Locate every blood parasite and identify its species.
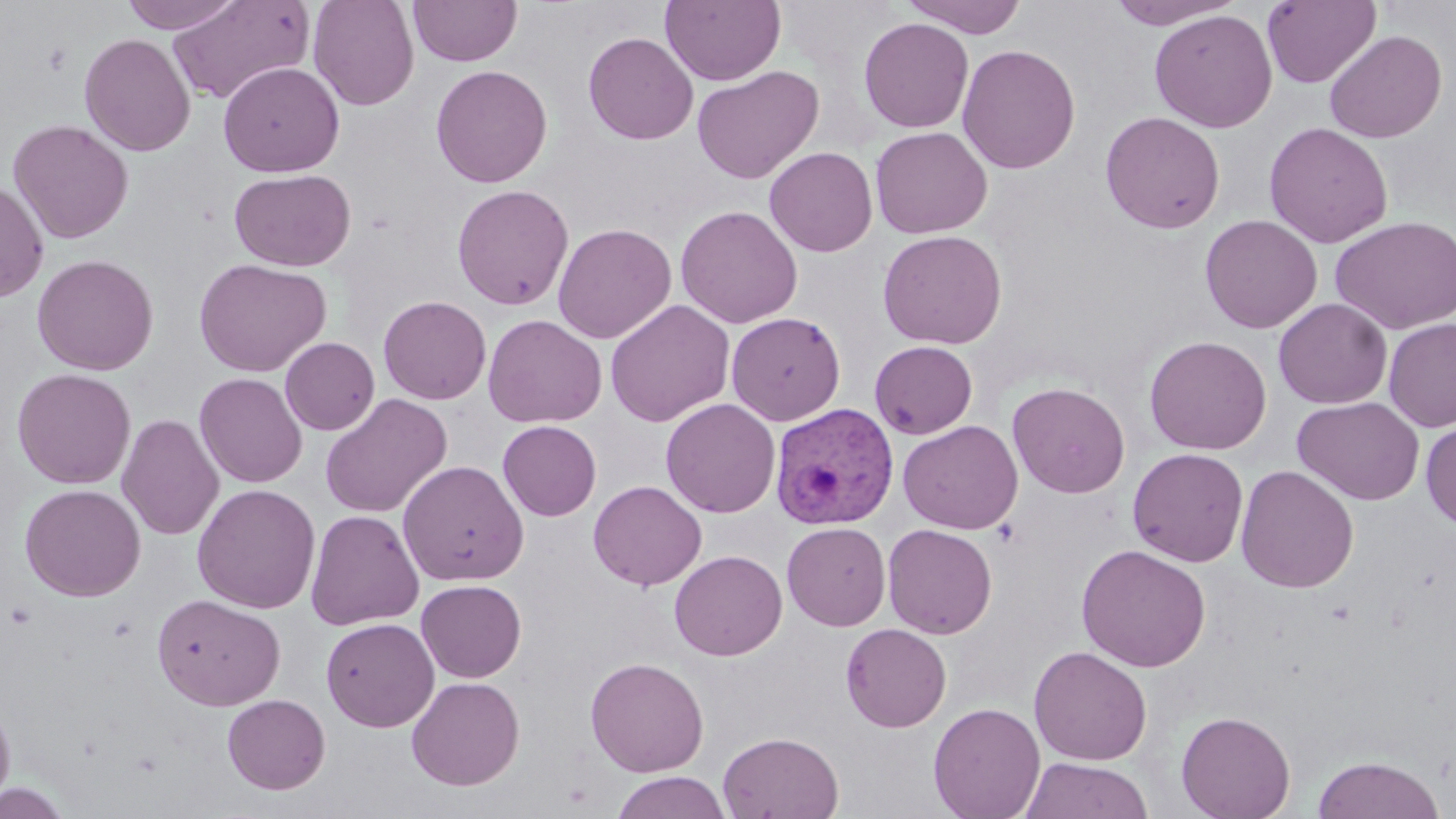
Approximate bounding boxes as (x1, y1, x2, y2) in pixels.
Plasmodium vivax-infected red blood cells: (770, 403, 899, 530).
No Plasmodium falciparum, Plasmodium ovale, Plasmodium malariae, Babesia divergens, or Trypanosoma brucei observed.

Summary:
  - Uninfected red blood cell locations: (117, 0, 247, 33), (167, 0, 314, 105), (307, 0, 420, 111), (408, 0, 522, 67), (660, 0, 786, 86), (902, 0, 1028, 38), (1106, 0, 1243, 29), (1262, 1, 1381, 88), (1149, 9, 1277, 133), (858, 17, 974, 134), (1324, 29, 1447, 143), (583, 31, 699, 145), (79, 33, 196, 157), (957, 44, 1080, 174), (218, 61, 344, 177), (430, 64, 552, 188), (691, 65, 825, 184), (1099, 111, 1225, 234), (7, 118, 134, 244), (1263, 122, 1393, 248), (869, 126, 993, 239), (764, 147, 878, 257), (229, 168, 356, 271), (0, 179, 49, 303), (452, 184, 574, 310), (675, 205, 803, 328), (1199, 214, 1322, 334), (1330, 215, 1456, 334), (552, 222, 677, 343), (877, 229, 1007, 349), (31, 254, 159, 375), (193, 258, 332, 377), (378, 295, 492, 405), (1273, 298, 1392, 409), (605, 299, 735, 427), (726, 311, 846, 426), (483, 314, 607, 428), (1384, 318, 1456, 432), (1143, 335, 1272, 455), (280, 337, 380, 435), (869, 340, 978, 439), (12, 368, 136, 488), (194, 373, 308, 488), (1007, 381, 1130, 498), (320, 393, 452, 518), (1292, 396, 1425, 505), (661, 398, 781, 518), (116, 414, 224, 540), (898, 419, 1023, 535), (1421, 419, 1456, 530), (497, 420, 602, 520), (1127, 447, 1249, 567), (397, 460, 529, 586), (1235, 464, 1359, 593), (588, 480, 707, 590), (19, 483, 146, 601), (192, 483, 321, 614), (305, 509, 425, 630), (782, 521, 892, 631), (882, 523, 998, 638), (1076, 543, 1211, 672), (669, 549, 788, 661), (416, 579, 527, 683), (151, 593, 286, 710), (321, 617, 440, 732), (841, 623, 951, 732), (1029, 645, 1152, 765), (585, 657, 709, 777), (407, 676, 525, 791), (0, 693, 16, 810), (222, 693, 331, 794), (928, 702, 1046, 819), (1176, 710, 1296, 819), (717, 731, 844, 818), (1312, 754, 1445, 819), (1022, 757, 1151, 818), (611, 771, 732, 819), (0, 782, 75, 819)
  - Slide-level diagnosis: Plasmodium vivax
  - Stain: May-Grünwald-Giemsa
  - Modality: light microscopy
  - Field of view: one of a larger specimen
  - Image size: 1456×819 pixels
  - Magnification: 1000x
  - Preparation: thin blood film